Outline each Plasmodium falciparum-infected red blood cell.
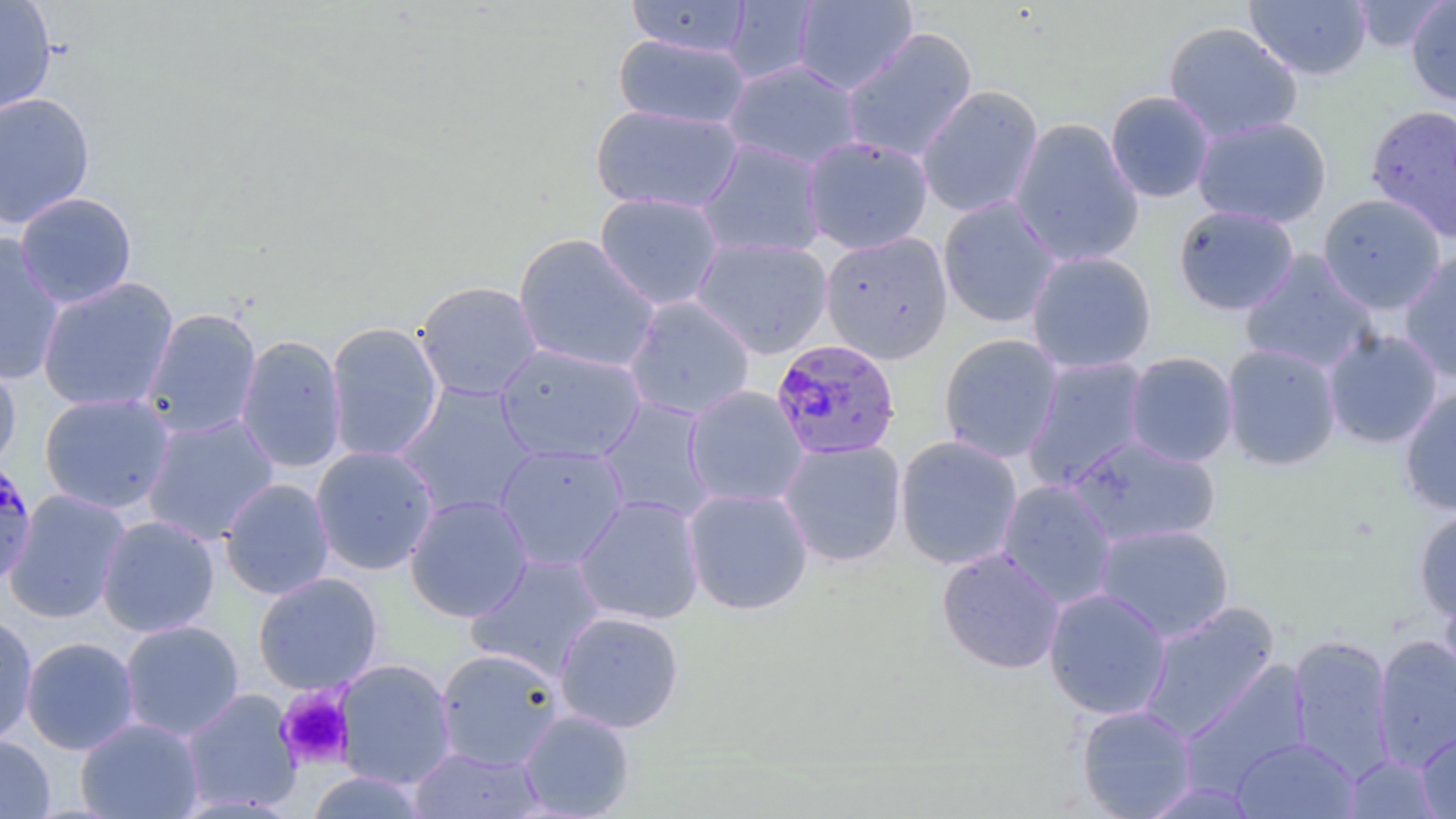

Approximate bounding boxes as (x1,y1)-(x2,y2) corner pairs in pixels.
Plasmodium falciparum-infected red blood cells: (770,339)-(901,461), (0,456)-(39,590).

Summary:
  - Uninfected red blood cell locations: (0,0)-(57,116), (626,0)-(752,58), (792,0)-(918,95), (1244,0)-(1373,81), (1349,0)-(1449,52), (722,1)-(820,85), (1406,1)-(1456,105), (1163,21)-(1303,143), (840,28)-(978,164), (614,35)-(751,130), (723,58)-(864,171), (915,85)-(1044,219), (1105,90)-(1216,203), (0,92)-(95,229), (1364,103)-(1456,242), (590,104)-(744,215), (1192,115)-(1332,228), (1008,118)-(1144,268), (802,136)-(934,254), (696,139)-(828,260), (15,192)-(137,309), (594,192)-(725,311), (1316,193)-(1447,314), (937,196)-(1061,329), (1173,204)-(1299,316), (820,231)-(953,364), (513,233)-(661,375), (0,234)-(66,387), (691,237)-(833,359), (1025,250)-(1157,374), (1399,250)-(1456,383), (1239,251)-(1380,375), (37,277)-(179,413), (414,280)-(543,401), (623,295)-(756,421), (141,308)-(262,440), (325,321)-(444,463), (1322,328)-(1443,449), (938,333)-(1063,463), (235,335)-(348,474), (495,342)-(647,465), (1221,343)-(1342,471), (1124,352)-(1239,468), (0,354)-(21,476), (1021,356)-(1152,491), (393,383)-(539,520), (683,385)-(810,508), (1399,387)-(1456,517), (38,392)-(176,515), (596,398)-(718,524), (141,413)-(280,545), (1066,434)-(1222,549), (894,435)-(1023,570), (777,439)-(907,567), (494,443)-(630,572), (311,446)-(440,575), (219,478)-(335,600), (996,479)-(1118,609), (682,487)-(814,616), (3,490)-(131,623), (405,494)-(533,622), (573,494)-(705,626), (1413,507)-(1456,624), (96,515)-(220,637), (1093,523)-(1235,643), (936,548)-(1066,674), (464,552)-(606,681), (253,572)-(383,695), (1437,582)-(1456,701), (1043,587)-(1172,720), (1138,602)-(1280,742), (0,611)-(38,747), (553,611)-(685,734), (119,620)-(244,741), (1287,634)-(1395,780), (1372,634)-(1456,773), (21,636)-(140,755), (436,648)-(564,771), (334,659)-(457,790), (1179,662)-(1311,795), (180,688)-(303,814), (1076,704)-(1198,819), (518,709)-(636,818), (75,717)-(205,818), (1416,725)-(1456,818), (0,734)-(55,818), (1230,737)-(1360,818), (409,746)-(546,818), (1341,753)-(1444,818), (305,770)-(430,818), (1138,781)-(1261,818)
  - Platelet locations: (275,687)-(354,770)
  - Slide-level diagnosis: Plasmodium falciparum
  - Preparation: thin blood smear
  - Stain: May-Grünwald-Giemsa
  - Modality: light microscopy
  - Image size: 1456×819 pixels
  - Field of view: one of a larger specimen
  - Magnification: 1000x